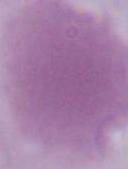 A red blood cell is shown. Captured at 1000x magnification. Micrograph.